Report the malaria status of this cell.
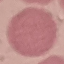

It is uninfected.

Automatically extracted cell patch, resized to 64 × 64 pixels. Photographed with a smartphone camera at the microscope eyepiece. Thin smear of blood. Giemsa stain.